Classify this cell by malaria status.
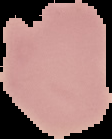

Parasitized.

From a thin blood film. Image is 112×139 pixels. Cell region segmented out of the field of view; the surrounding area is masked to black.